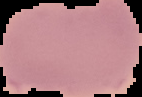

Summary:
  - Image size: 142×97 pixels
  - Preparation: thin blood film
  - Malaria status: uninfected
  - Image type: segmented cell region with the area outside set to black